State the blood parasite species.
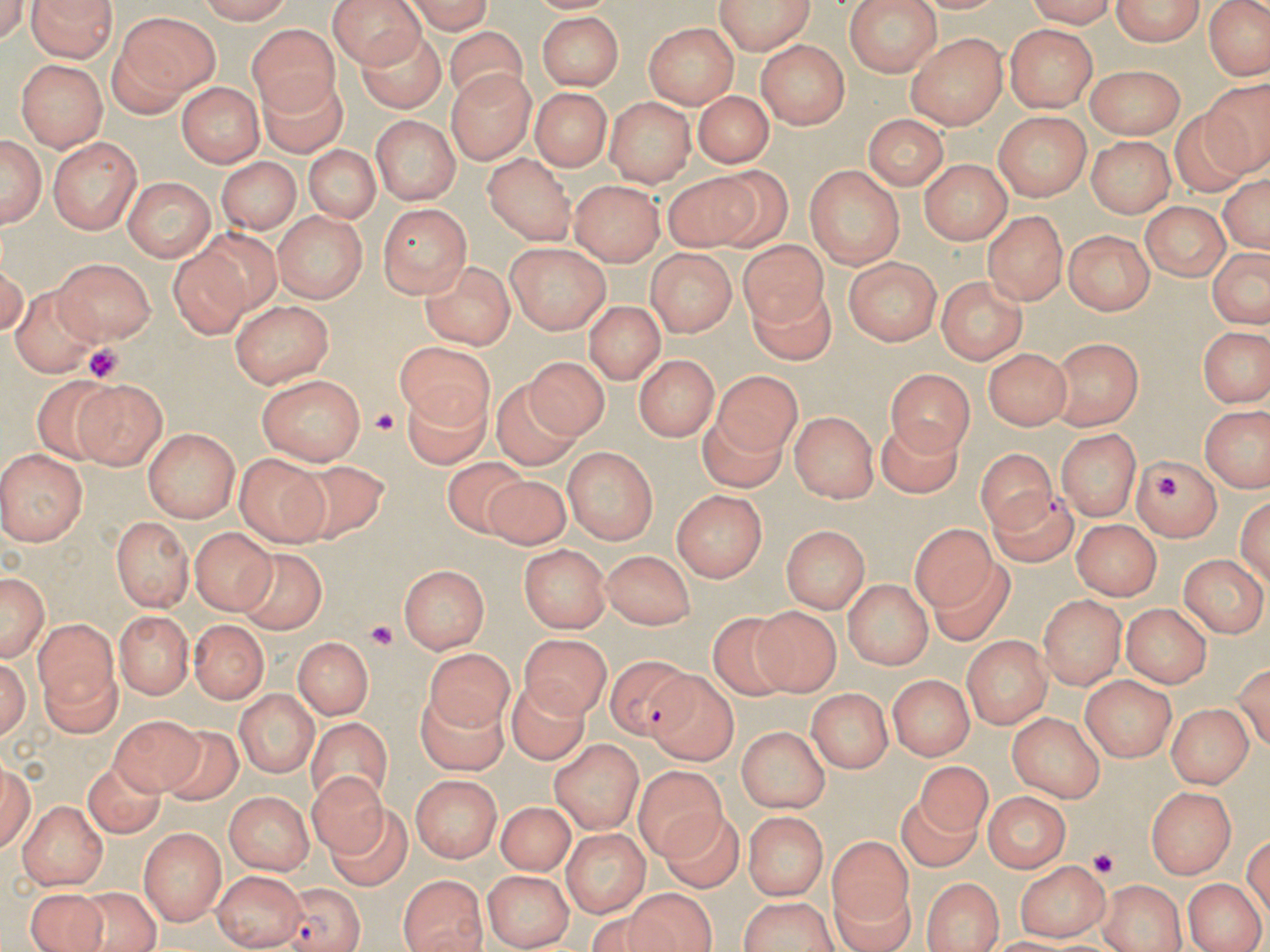

Plasmodium falciparum.

platelet_locations: 'approximate bounding boxes as named x1/y1/x2/y2 corners in pixels: (x1=86, y1=346, x2=126, y2=379), (x1=369, y1=408, x2=395, y2=437), (x1=1155, y1=472, x2=1186, y2=499), (x1=367, y1=622, x2=396, y2=654), (x1=1086, y1=849, x2=1119, y2=877)'
uninfected_red_blood_cell_locations: 'approximate bounding boxes as named x1/y1/x2/y2 corners in pixels: (x1=31, y1=0, x2=115, y2=63), (x1=190, y1=0, x2=300, y2=22), (x1=326, y1=0, x2=429, y2=69), (x1=401, y1=0, x2=497, y2=32), (x1=717, y1=0, x2=817, y2=53), (x1=844, y1=0, x2=942, y2=77), (x1=1106, y1=0, x2=1208, y2=50), (x1=1208, y1=0, x2=1268, y2=85), (x1=116, y1=12, x2=218, y2=102), (x1=534, y1=13, x2=623, y2=91), (x1=246, y1=22, x2=335, y2=113), (x1=354, y1=23, x2=445, y2=116), (x1=641, y1=23, x2=737, y2=108), (x1=1004, y1=25, x2=1098, y2=111), (x1=447, y1=29, x2=529, y2=108), (x1=903, y1=34, x2=1009, y2=128), (x1=755, y1=40, x2=847, y2=128), (x1=15, y1=60, x2=105, y2=150), (x1=1084, y1=64, x2=1183, y2=137), (x1=258, y1=67, x2=349, y2=161), (x1=449, y1=72, x2=533, y2=164), (x1=1197, y1=77, x2=1270, y2=179), (x1=177, y1=80, x2=267, y2=167), (x1=531, y1=86, x2=611, y2=169), (x1=691, y1=91, x2=776, y2=166), (x1=608, y1=97, x2=697, y2=188), (x1=1168, y1=110, x2=1259, y2=196), (x1=993, y1=111, x2=1090, y2=200), (x1=370, y1=116, x2=461, y2=203), (x1=866, y1=117, x2=945, y2=185), (x1=0, y1=132, x2=47, y2=232), (x1=47, y1=136, x2=144, y2=234), (x1=1086, y1=136, x2=1177, y2=215), (x1=305, y1=144, x2=379, y2=226), (x1=484, y1=152, x2=576, y2=244), (x1=215, y1=156, x2=301, y2=234), (x1=921, y1=160, x2=1008, y2=246), (x1=805, y1=164, x2=907, y2=268), (x1=710, y1=168, x2=795, y2=251), (x1=1219, y1=169, x2=1269, y2=259), (x1=664, y1=173, x2=761, y2=254), (x1=124, y1=177, x2=213, y2=262), (x1=571, y1=179, x2=663, y2=266), (x1=1139, y1=200, x2=1232, y2=280), (x1=378, y1=204, x2=472, y2=298), (x1=985, y1=210, x2=1067, y2=305), (x1=274, y1=211, x2=366, y2=302), (x1=201, y1=225, x2=286, y2=313), (x1=1066, y1=229, x2=1158, y2=316), (x1=738, y1=237, x2=830, y2=331), (x1=506, y1=241, x2=611, y2=332), (x1=168, y1=244, x2=253, y2=340), (x1=647, y1=249, x2=735, y2=335), (x1=1204, y1=249, x2=1270, y2=331), (x1=421, y1=254, x2=518, y2=345), (x1=56, y1=257, x2=155, y2=345), (x1=842, y1=258, x2=943, y2=343), (x1=938, y1=275, x2=1026, y2=365), (x1=746, y1=277, x2=834, y2=366), (x1=11, y1=285, x2=107, y2=379), (x1=231, y1=301, x2=335, y2=388), (x1=584, y1=301, x2=663, y2=387), (x1=1201, y1=328, x2=1266, y2=406), (x1=1053, y1=335, x2=1144, y2=429), (x1=396, y1=343, x2=494, y2=433), (x1=984, y1=347, x2=1071, y2=431), (x1=632, y1=355, x2=721, y2=440), (x1=522, y1=357, x2=613, y2=440), (x1=883, y1=368, x2=970, y2=461), (x1=716, y1=371, x2=804, y2=457), (x1=32, y1=374, x2=134, y2=464), (x1=257, y1=374, x2=363, y2=464), (x1=76, y1=377, x2=166, y2=468), (x1=494, y1=378, x2=585, y2=471), (x1=406, y1=381, x2=493, y2=471), (x1=1200, y1=402, x2=1270, y2=492), (x1=697, y1=404, x2=787, y2=491), (x1=791, y1=409, x2=879, y2=501), (x1=875, y1=415, x2=963, y2=501), (x1=1171, y1=415, x2=1256, y2=506), (x1=144, y1=428, x2=240, y2=521), (x1=1055, y1=431, x2=1142, y2=520), (x1=561, y1=444, x2=657, y2=544), (x1=975, y1=448, x2=1058, y2=536), (x1=0, y1=450, x2=85, y2=545), (x1=237, y1=451, x2=331, y2=546), (x1=438, y1=453, x2=534, y2=538), (x1=1132, y1=453, x2=1223, y2=537), (x1=275, y1=462, x2=392, y2=543), (x1=480, y1=477, x2=574, y2=553), (x1=673, y1=489, x2=769, y2=580), (x1=1236, y1=489, x2=1270, y2=590), (x1=109, y1=516, x2=190, y2=610), (x1=1070, y1=518, x2=1163, y2=598), (x1=907, y1=521, x2=997, y2=613), (x1=781, y1=524, x2=872, y2=613), (x1=191, y1=528, x2=275, y2=615), (x1=516, y1=542, x2=611, y2=632), (x1=600, y1=547, x2=695, y2=629), (x1=233, y1=548, x2=333, y2=637), (x1=1181, y1=554, x2=1265, y2=636), (x1=930, y1=555, x2=1014, y2=647), (x1=399, y1=564, x2=489, y2=653), (x1=1, y1=567, x2=50, y2=664), (x1=840, y1=579, x2=935, y2=669), (x1=1038, y1=595, x2=1127, y2=689), (x1=1122, y1=603, x2=1211, y2=687), (x1=751, y1=606, x2=841, y2=698), (x1=112, y1=609, x2=189, y2=697), (x1=706, y1=611, x2=799, y2=699), (x1=188, y1=617, x2=267, y2=702), (x1=33, y1=618, x2=117, y2=728), (x1=519, y1=632, x2=608, y2=720), (x1=960, y1=634, x2=1054, y2=726), (x1=296, y1=638, x2=370, y2=719), (x1=423, y1=647, x2=518, y2=733), (x1=644, y1=664, x2=736, y2=763), (x1=507, y1=673, x2=588, y2=767), (x1=1081, y1=674, x2=1176, y2=762), (x1=886, y1=675, x2=971, y2=762), (x1=414, y1=686, x2=510, y2=775), (x1=805, y1=687, x2=894, y2=772), (x1=233, y1=688, x2=318, y2=777), (x1=1165, y1=704, x2=1253, y2=786), (x1=108, y1=711, x2=207, y2=798), (x1=1008, y1=711, x2=1104, y2=803), (x1=307, y1=718, x2=389, y2=805), (x1=735, y1=725, x2=827, y2=811), (x1=156, y1=727, x2=246, y2=806), (x1=549, y1=738, x2=646, y2=833), (x1=915, y1=758, x2=996, y2=838), (x1=82, y1=761, x2=163, y2=837), (x1=631, y1=768, x2=726, y2=867), (x1=310, y1=770, x2=389, y2=859), (x1=411, y1=777, x2=500, y2=864), (x1=1148, y1=785, x2=1237, y2=881), (x1=893, y1=793, x2=982, y2=871), (x1=227, y1=794, x2=312, y2=874), (x1=983, y1=794, x2=1068, y2=873), (x1=498, y1=799, x2=572, y2=876), (x1=19, y1=802, x2=112, y2=890), (x1=328, y1=804, x2=414, y2=891), (x1=658, y1=806, x2=742, y2=890), (x1=741, y1=811, x2=832, y2=897), (x1=139, y1=826, x2=225, y2=923), (x1=559, y1=829, x2=649, y2=915), (x1=825, y1=836, x2=911, y2=927), (x1=1016, y1=860, x2=1110, y2=941), (x1=209, y1=869, x2=306, y2=947), (x1=479, y1=869, x2=576, y2=946), (x1=399, y1=874, x2=487, y2=952), (x1=923, y1=875, x2=1004, y2=952), (x1=1185, y1=878, x2=1262, y2=952), (x1=1103, y1=880, x2=1191, y2=952), (x1=27, y1=887, x2=108, y2=952), (x1=65, y1=889, x2=160, y2=952), (x1=620, y1=889, x2=720, y2=952), (x1=734, y1=895, x2=841, y2=952)'
preparation: thin blood smear
field_of_view: one of a larger specimen
magnification: 1000x
modality: light microscopy
image_size: 1270×952 pixels
plasmodium_falciparum_infected_red_blood_cell_locations: 'approximate bounding boxes as named x1/y1/x2/y2 corners in pixels: (x1=987, y1=486, x2=1081, y2=569), (x1=606, y1=655, x2=699, y2=743), (x1=276, y1=886, x2=368, y2=952)'
stain: May-Grünwald-Giemsa